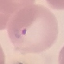
{
  "malaria_status": "parasitized",
  "image_type": "cell patch, automatically extracted from a larger field of view and resized to 64 × 64 pixels",
  "preparation": "thin blood film",
  "stain": "Giemsa",
  "capture": "smartphone through the microscope eyepiece"
}